Identify the preparation type.
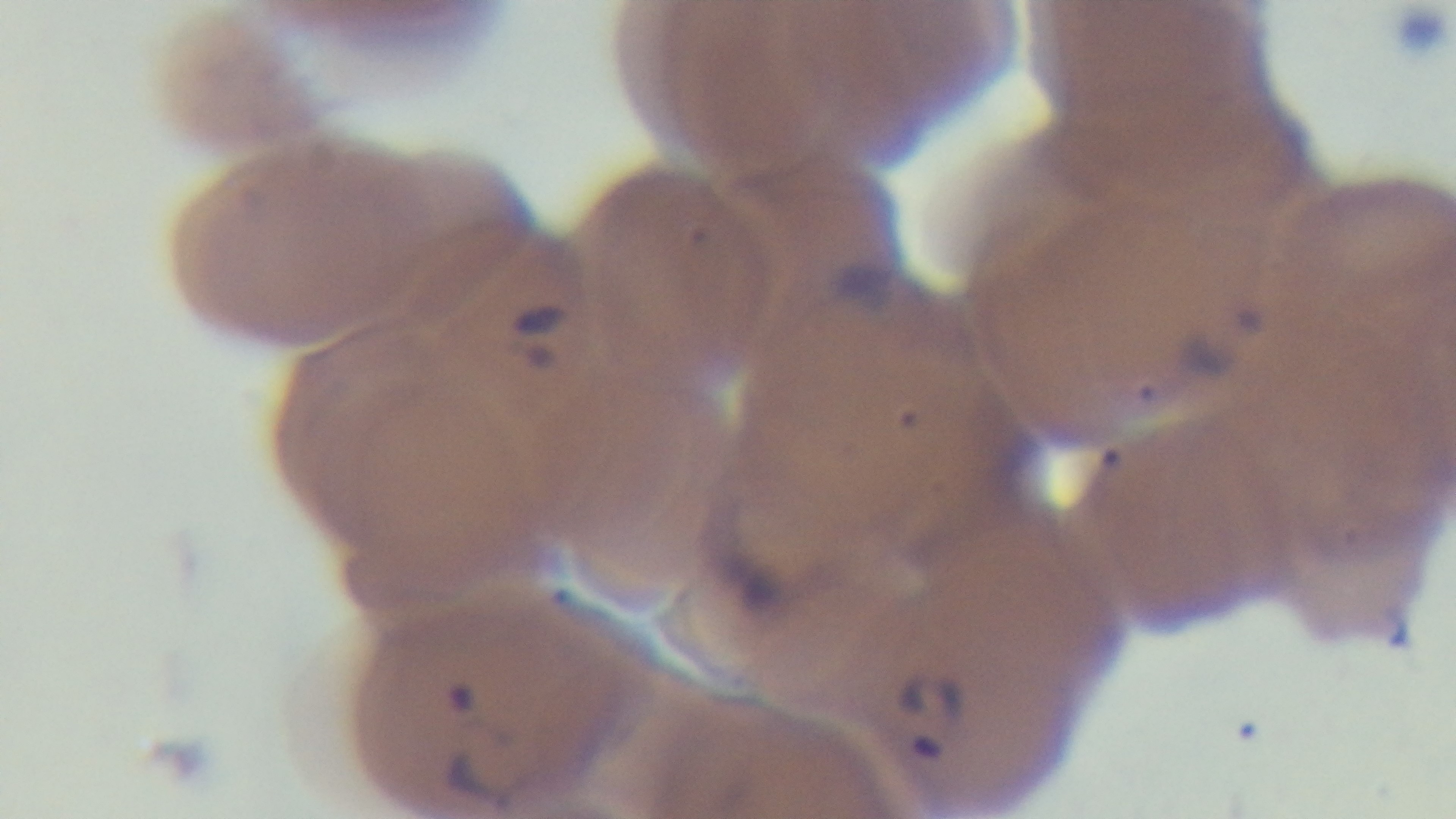
A thin smear.

Giemsa-stained. Malaria status: positive. Oil-immersion objective, 100x. One field from the slide. Photomicrograph. Mounted 4K digital camera.